Report the malaria status of this cell.
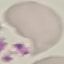

It is uninfected.

Summary:
  - Capture: smartphone camera at the microscope eyepiece
  - Preparation: thin blood smear
  - Stain: Giemsa
  - Image type: cell patch, automatically extracted from a larger field of view and resized to 64 × 64 pixels